Describe the morphology of the red blood cells.
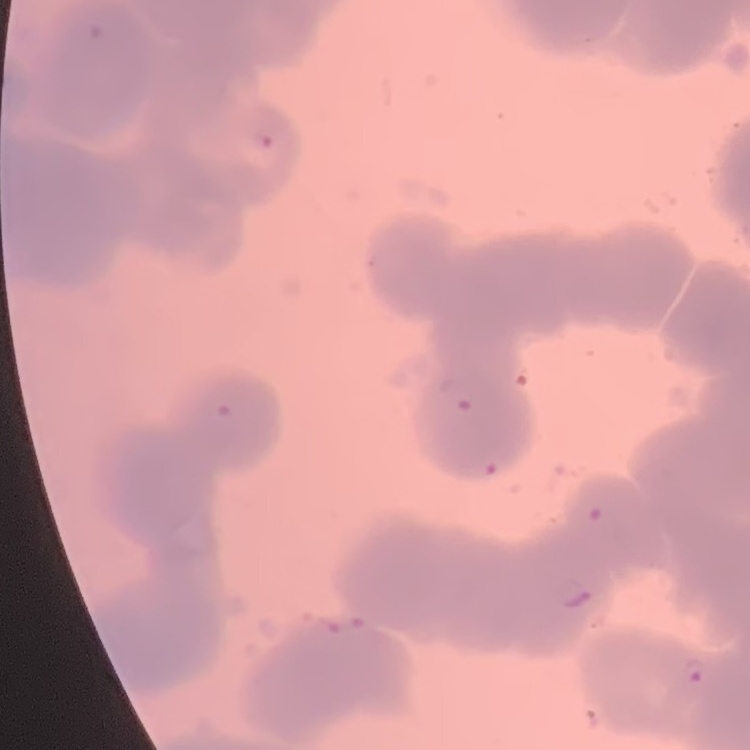
They show rouleaux formation.

preparation: thin blood smear
stain: Field's or Giemsa
image_type: one tile cut from a larger photomicrograph